Comment on the morphology of the erythrocytes.
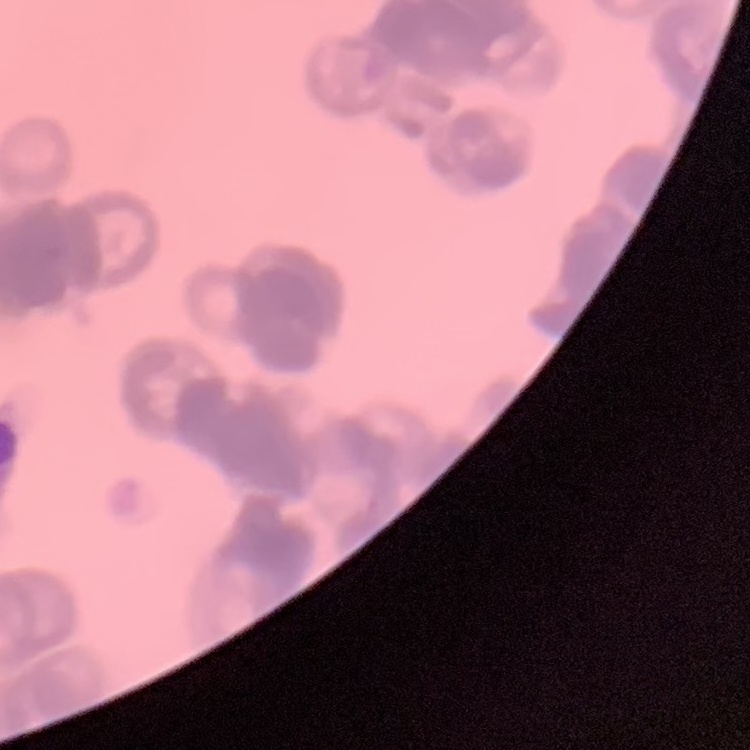

Rouleaux formation.

Summary:
  - Preparation: thin blood smear
  - Image type: square crop of a larger photomicrograph
  - Stain: Field's or Giemsa